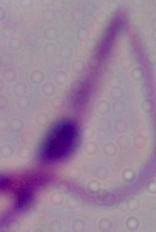
Summary:
  - Identification: Leishmania
  - Magnification: 1000x
  - Modality: photomicrograph